Assess for Plasmodium parasites.
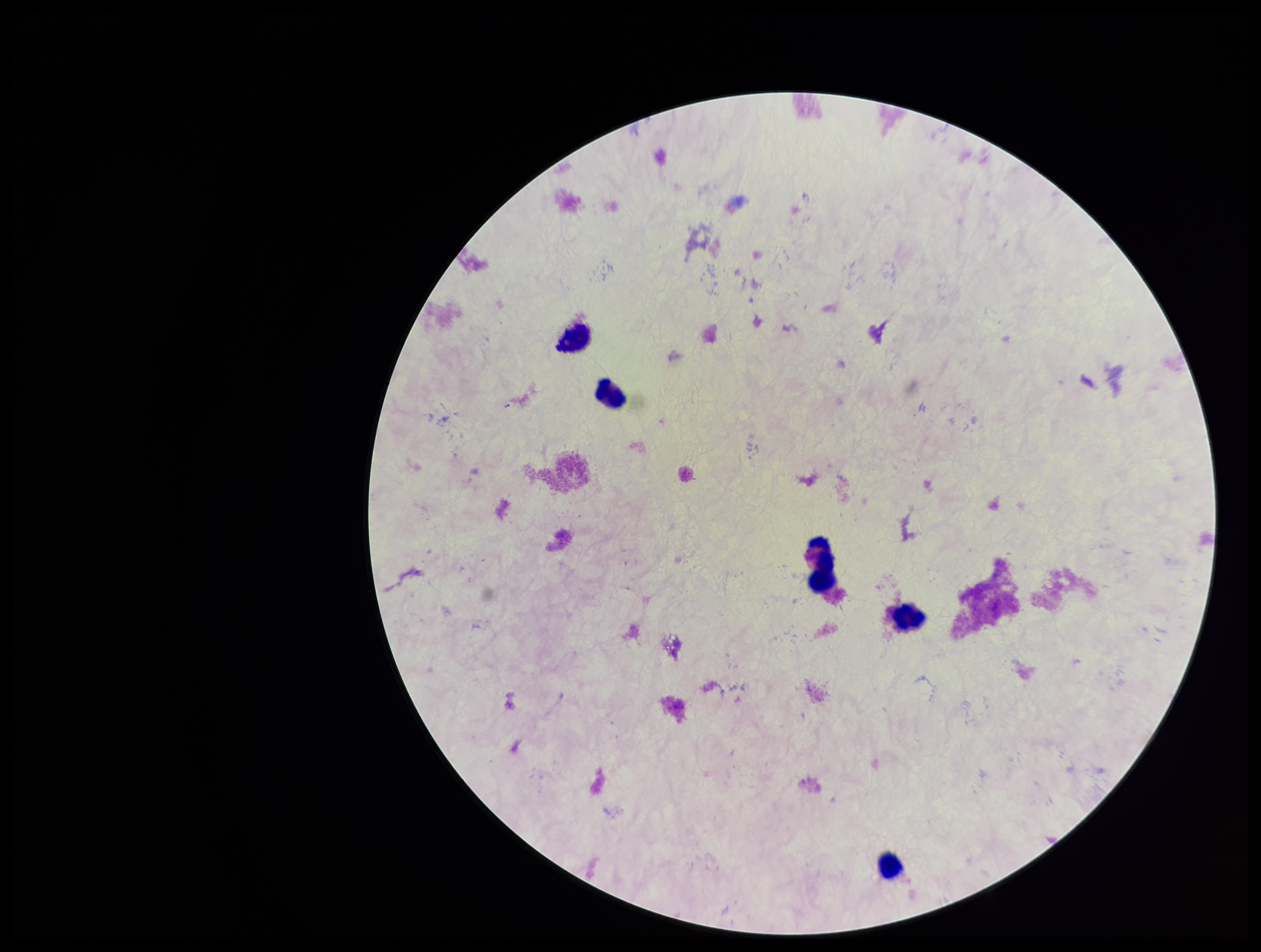
None identified.

patient malaria status = negative
leukocyte count = 5
preparation = thick smear
image size = 1261×952 pixels
capture = smartphone photograph through the microscope eyepiece
parasite count = 0
stain = Giemsa
field of view = single